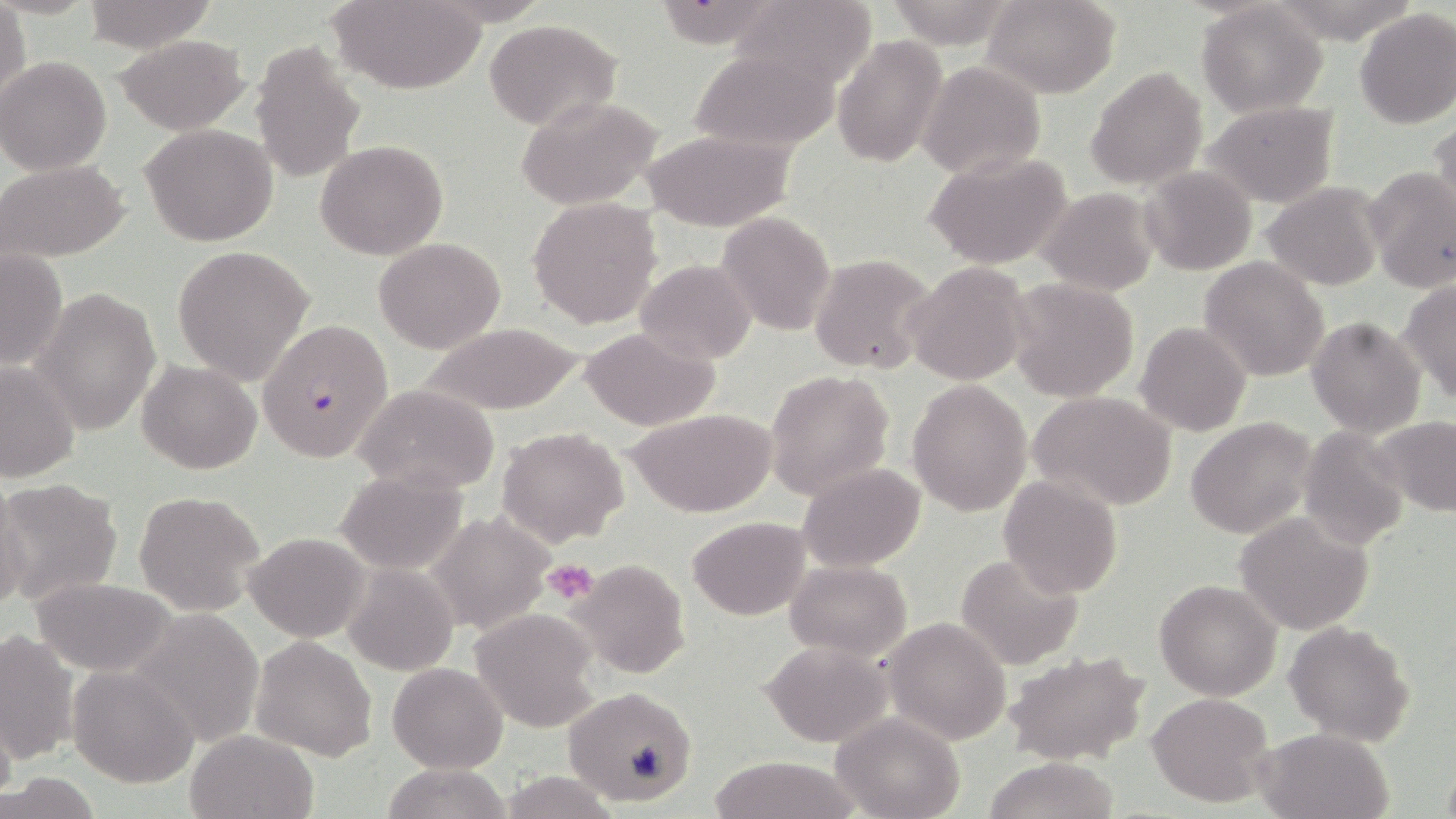

slide_level_diagnosis: Plasmodium falciparum
image_size: 1456×819 pixels
magnification: 1000x
uninfected_red_blood_cell_locations: 'approximate bounding boxes as (x1, y1, x2, y2) in pixels: (82, 0, 215, 54), (329, 0, 485, 92), (981, 0, 1121, 97), (734, 1, 876, 91), (1196, 1, 1330, 117), (0, 2, 30, 109), (1354, 7, 1456, 128), (484, 19, 622, 131), (117, 34, 249, 134), (832, 35, 948, 167), (250, 38, 367, 186), (690, 47, 837, 153), (0, 58, 111, 175), (917, 61, 1046, 181), (1085, 65, 1209, 191), (516, 94, 666, 211), (1200, 101, 1339, 207), (1430, 116, 1456, 224), (139, 124, 278, 246), (641, 129, 795, 231), (316, 139, 447, 259), (925, 152, 1074, 270), (1, 159, 129, 263), (1140, 165, 1257, 277), (1366, 167, 1456, 293), (1261, 182, 1384, 292), (1038, 188, 1160, 294), (527, 197, 663, 330), (716, 212, 835, 335), (374, 238, 506, 354), (172, 246, 314, 385), (0, 250, 67, 371), (809, 253, 936, 374), (1198, 257, 1330, 383), (634, 259, 757, 366), (905, 262, 1029, 385), (1005, 277, 1139, 401), (1400, 281, 1456, 402), (33, 287, 162, 435), (1307, 316, 1426, 436), (1135, 321, 1251, 436), (416, 323, 586, 415), (579, 326, 719, 430), (138, 359, 260, 474), (0, 360, 79, 483), (763, 369, 895, 501), (907, 380, 1034, 518), (353, 383, 501, 494), (1031, 391, 1177, 511), (626, 406, 777, 517), (1373, 415, 1456, 518), (1186, 417, 1317, 538), (497, 426, 629, 547), (1298, 427, 1410, 548), (798, 463, 926, 570), (337, 469, 469, 575), (997, 473, 1123, 599), (1, 479, 31, 615), (0, 480, 122, 611), (133, 490, 267, 615), (428, 511, 553, 637), (1232, 511, 1374, 637), (686, 516, 810, 620), (245, 531, 370, 642), (955, 552, 1084, 670), (567, 559, 690, 678), (785, 560, 912, 661), (341, 561, 458, 678), (1155, 579, 1282, 700), (29, 580, 173, 673), (125, 607, 267, 747), (468, 608, 599, 731), (885, 618, 1012, 745), (1284, 620, 1414, 747), (0, 630, 79, 766), (249, 635, 379, 761), (761, 641, 892, 747), (1003, 649, 1151, 766), (387, 662, 507, 772), (68, 665, 201, 787), (562, 686, 698, 806), (1147, 691, 1276, 808), (0, 709, 18, 802), (832, 712, 966, 819), (1256, 727, 1393, 819), (184, 730, 317, 819), (708, 756, 859, 818), (982, 757, 1123, 819), (378, 761, 515, 819), (2, 772, 105, 817), (498, 772, 623, 817)'
field_of_view: one of a larger specimen
stain: May-Grünwald-Giemsa
preparation: thin blood film
platelet_locations: 'approximate bounding boxes as (x1, y1, x2, y2) in pixels: (543, 559, 597, 605)'
plasmodium_falciparum_infected_red_blood_cell_locations: 'approximate bounding boxes as (x1, y1, x2, y2) in pixels: (257, 318, 395, 464)'
modality: optical microscopy